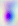
400x magnification. Toxoplasma gondii is seen. Photomicrograph.